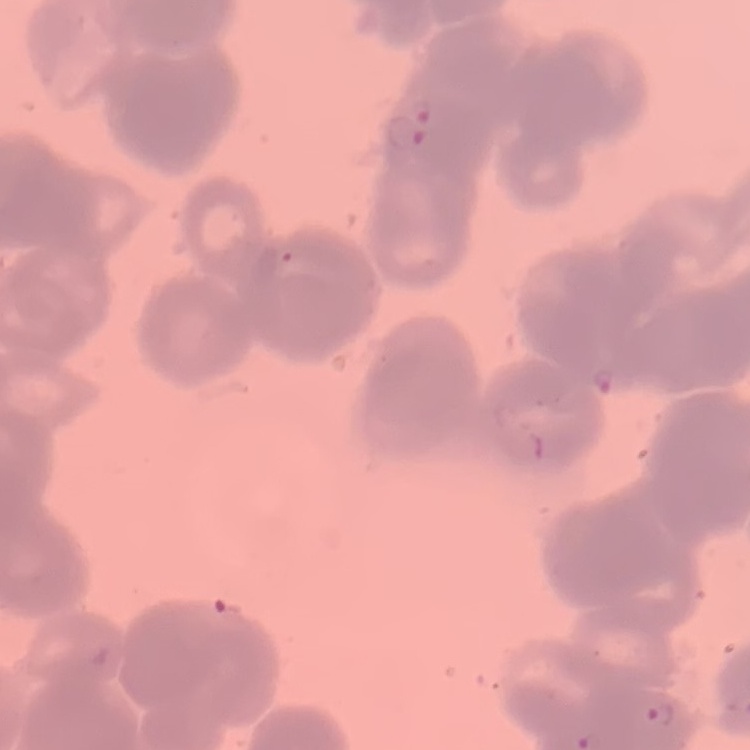

{
  "red_blood_cell_morphology": "rouleaux formation",
  "stain": "Field's or Giemsa",
  "image_type": "one tile cut from a larger photomicrograph",
  "preparation": "thin peripheral smear"
}